Report the malaria status of this cell.
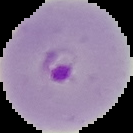

It is parasitized.

Summary:
  - Image type: segmented cell region on a black background
  - Image size: 133×133 pixels
  - Preparation: thin blood smear